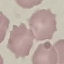
result = negative for malaria parasites
capture = smartphone through the microscope eyepiece
stain = Giemsa
image type = automatically extracted cell patch, resized to 64 × 64 pixels
preparation = thin blood film